Give the position of every Plasmodium parasite visible.
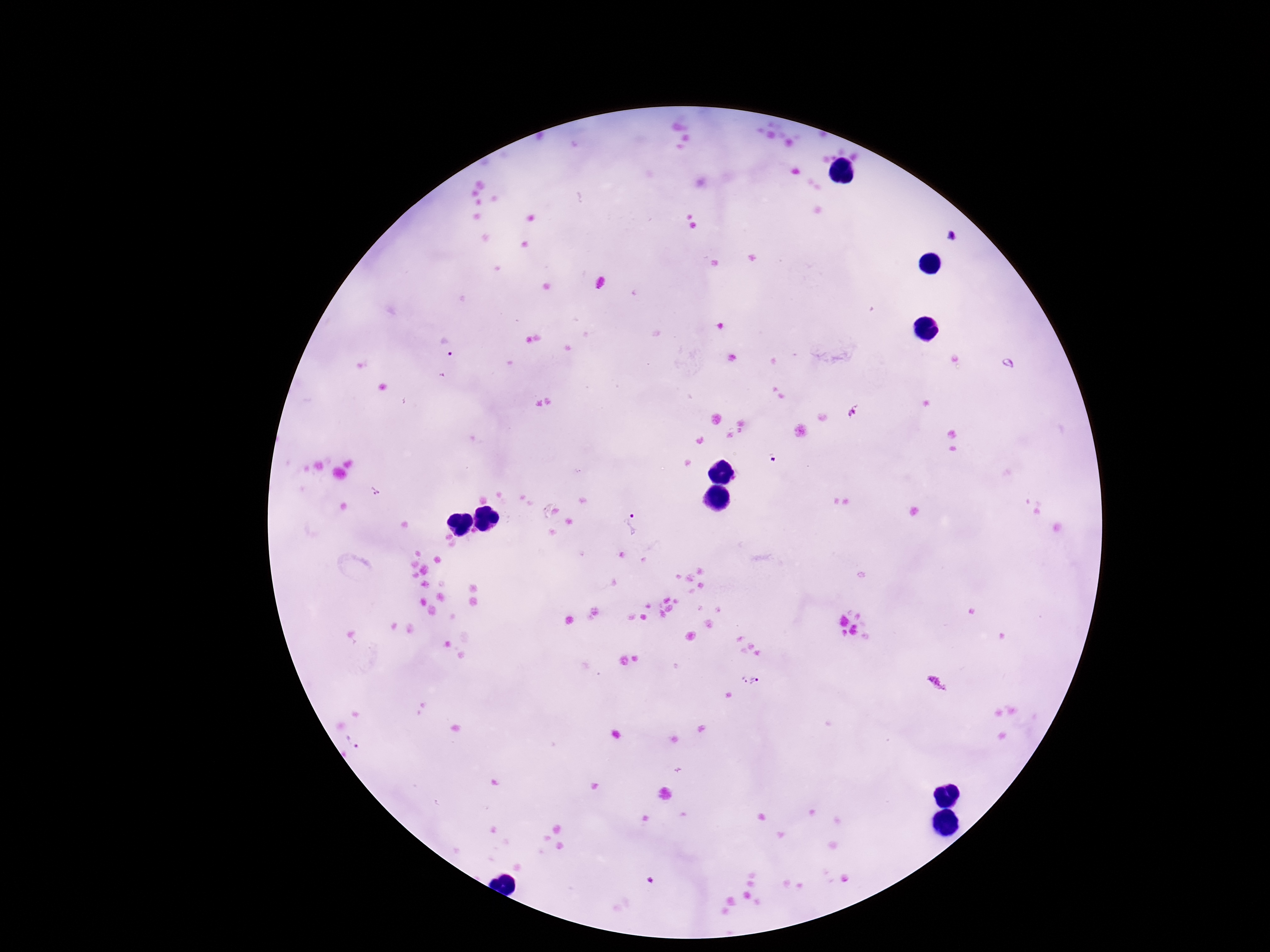
Approximate centers as (x, y) in pixels.
Plasmodium parasites: (449, 350), (855, 411), (630, 526), (751, 679), (353, 740).

Summary:
  - Image size: 1270×952 pixels
  - Preparation: thick peripheral-blood smear
  - Field of view: single
  - Capture: smartphone camera through the microscope eyepiece
  - Stain: Giemsa
  - Magnification: 100x
  - Patient malaria status: positive